Assess the morphology of the erythrocytes.
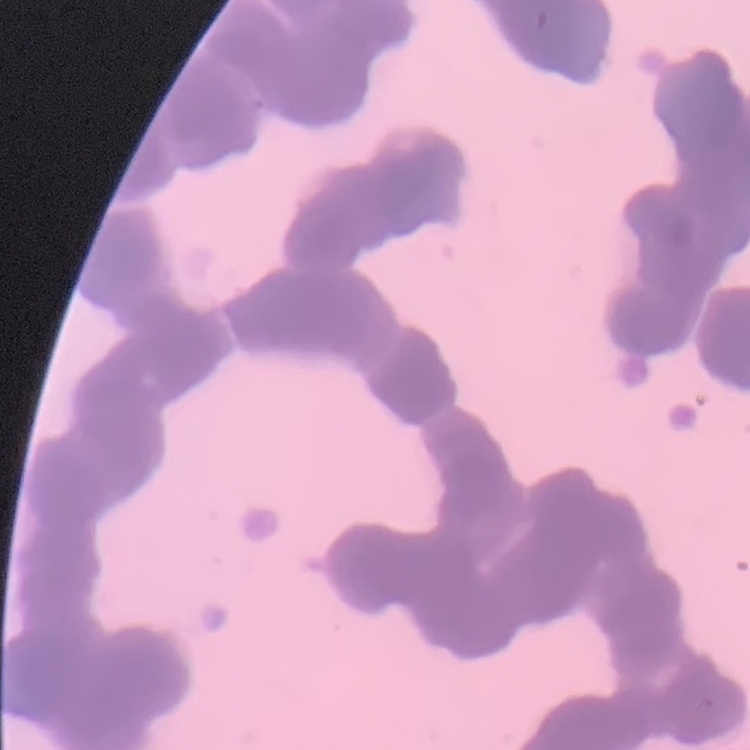
Rouleaux formation.

preparation: thin blood smear
stain: Field's or Giemsa
image_type: one tile cut from a larger photomicrograph